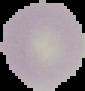 Malaria status: uninfected. Image is 85×91 pixels. Cell region segmented out of the field of view; the surrounding area is masked to black. From a thin blood smear.